Assess this cell for malaria.
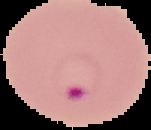

Parasitized.

Summary:
  - Image type: cell region segmented out of the field of view; surrounding area masked to black
  - Preparation: thin blood film
  - Image size: 151×130 pixels